State which parasite is depicted.
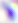

This is Toxoplasma gondii.

{
  "modality": "photomicrograph",
  "magnification": "400x"
}